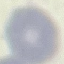 Malaria status: uninfected. Acquired by smartphone through the microscope eyepiece. Thin smear of blood. Automatically extracted cell patch, resized to 64 × 64 pixels. Giemsa-stained preparation.